Name the parasite shown.
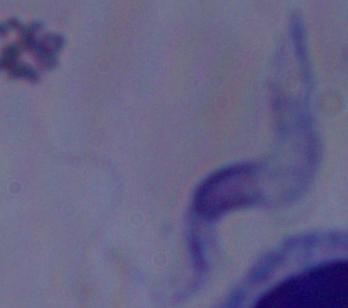

A trypanosome.

Photomicrograph. Captured at 1000x magnification.